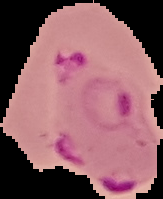

image_size: 163×199 pixels
result: Plasmodium parasites detected
preparation: thin blood film
image_type: segmented cell region with the area outside set to black